Report the malaria status of this cell.
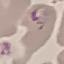

Parasitized.

Summary:
  - Preparation: thin blood smear
  - Capture: smartphone camera at the microscope eyepiece
  - Image type: automatically extracted cell patch, resized to 64 × 64 pixels
  - Stain: Giemsa